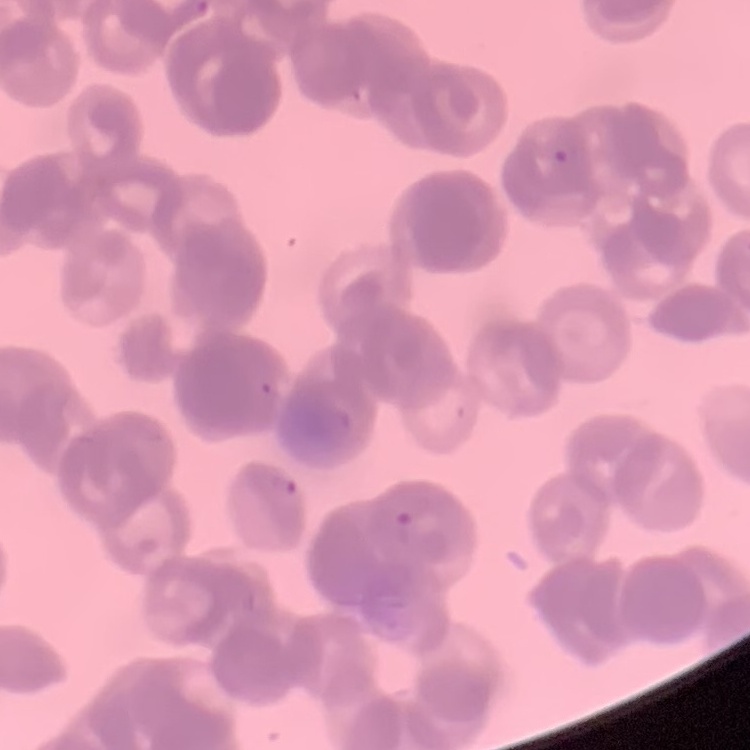

red blood cell morphology = rouleaux formation
stain = Field's or Giemsa
preparation = thin blood smear
image type = one tile cut from a larger photomicrograph